Outline each blood parasite and name the species.
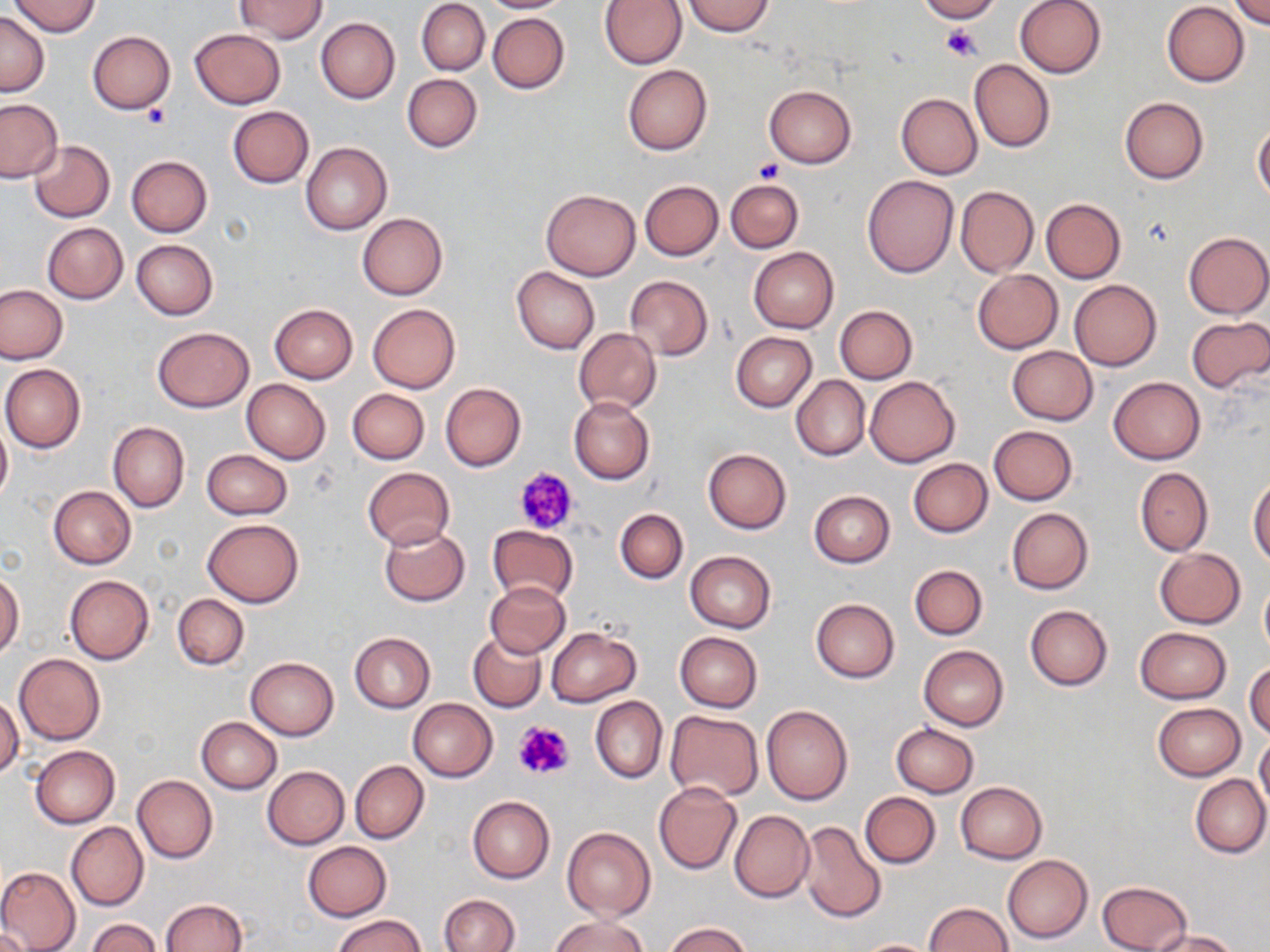

No blood parasites observed.

Approximate bounding boxes as named x1/y1/x2/y2 corners in pixels. Uninfected red blood cell locations: (x1=10, y1=0, x2=101, y2=36), (x1=233, y1=0, x2=328, y2=41), (x1=481, y1=0, x2=576, y2=12), (x1=917, y1=0, x2=1000, y2=23), (x1=1015, y1=0, x2=1107, y2=78), (x1=1232, y1=0, x2=1269, y2=28), (x1=417, y1=1, x2=489, y2=75), (x1=598, y1=1, x2=687, y2=68), (x1=683, y1=1, x2=775, y2=36), (x1=1162, y1=2, x2=1249, y2=86), (x1=0, y1=13, x2=49, y2=96), (x1=488, y1=13, x2=569, y2=93), (x1=315, y1=17, x2=400, y2=103), (x1=190, y1=27, x2=285, y2=109), (x1=87, y1=30, x2=175, y2=115), (x1=969, y1=59, x2=1054, y2=152), (x1=623, y1=65, x2=712, y2=154), (x1=402, y1=73, x2=481, y2=152), (x1=764, y1=85, x2=856, y2=167), (x1=896, y1=93, x2=982, y2=179), (x1=1118, y1=97, x2=1208, y2=184), (x1=0, y1=98, x2=63, y2=183), (x1=228, y1=107, x2=314, y2=188), (x1=1253, y1=123, x2=1270, y2=202), (x1=28, y1=140, x2=115, y2=222), (x1=301, y1=142, x2=392, y2=235), (x1=126, y1=155, x2=212, y2=236), (x1=863, y1=175, x2=959, y2=278), (x1=725, y1=179, x2=804, y2=253), (x1=640, y1=180, x2=723, y2=260), (x1=955, y1=185, x2=1037, y2=278), (x1=541, y1=188, x2=640, y2=280), (x1=1041, y1=198, x2=1125, y2=283), (x1=358, y1=212, x2=447, y2=300), (x1=41, y1=222, x2=128, y2=304), (x1=1183, y1=231, x2=1269, y2=319), (x1=131, y1=240, x2=218, y2=320), (x1=750, y1=247, x2=838, y2=333), (x1=511, y1=267, x2=600, y2=355), (x1=973, y1=269, x2=1063, y2=354), (x1=625, y1=276, x2=712, y2=360), (x1=1069, y1=279, x2=1162, y2=371), (x1=0, y1=284, x2=69, y2=364), (x1=368, y1=303, x2=461, y2=392), (x1=269, y1=304, x2=357, y2=384), (x1=835, y1=305, x2=917, y2=383), (x1=1186, y1=316, x2=1270, y2=393), (x1=152, y1=327, x2=253, y2=412), (x1=574, y1=328, x2=661, y2=413), (x1=731, y1=333, x2=816, y2=411), (x1=1007, y1=346, x2=1097, y2=426), (x1=1, y1=364, x2=85, y2=452), (x1=791, y1=375, x2=869, y2=461), (x1=865, y1=375, x2=960, y2=468), (x1=1109, y1=376, x2=1205, y2=464), (x1=242, y1=378, x2=331, y2=464), (x1=439, y1=382, x2=526, y2=472), (x1=347, y1=388, x2=429, y2=464), (x1=568, y1=397, x2=654, y2=484), (x1=0, y1=419, x2=11, y2=504), (x1=108, y1=422, x2=189, y2=512), (x1=988, y1=426, x2=1078, y2=505), (x1=703, y1=448, x2=791, y2=534), (x1=202, y1=449, x2=292, y2=519), (x1=908, y1=459, x2=992, y2=538), (x1=1134, y1=466, x2=1212, y2=556), (x1=362, y1=467, x2=455, y2=549), (x1=1249, y1=476, x2=1270, y2=567), (x1=49, y1=487, x2=136, y2=569), (x1=809, y1=491, x2=895, y2=567), (x1=614, y1=508, x2=688, y2=583), (x1=1007, y1=508, x2=1093, y2=594), (x1=202, y1=519, x2=303, y2=607), (x1=380, y1=522, x2=470, y2=606), (x1=488, y1=525, x2=578, y2=605), (x1=1154, y1=548, x2=1247, y2=628), (x1=686, y1=552, x2=775, y2=633), (x1=910, y1=565, x2=987, y2=640), (x1=0, y1=571, x2=24, y2=659), (x1=65, y1=575, x2=154, y2=664), (x1=1259, y1=577, x2=1270, y2=660), (x1=485, y1=581, x2=570, y2=658), (x1=172, y1=594, x2=248, y2=670), (x1=811, y1=598, x2=899, y2=683), (x1=1025, y1=604, x2=1112, y2=690), (x1=1135, y1=626, x2=1231, y2=703), (x1=547, y1=627, x2=641, y2=707), (x1=467, y1=631, x2=546, y2=712), (x1=674, y1=631, x2=762, y2=713), (x1=350, y1=632, x2=435, y2=711), (x1=919, y1=645, x2=1009, y2=730), (x1=14, y1=654, x2=105, y2=745), (x1=245, y1=657, x2=338, y2=741), (x1=1247, y1=661, x2=1270, y2=742), (x1=0, y1=696, x2=23, y2=779), (x1=591, y1=696, x2=667, y2=783), (x1=408, y1=698, x2=497, y2=781), (x1=1153, y1=702, x2=1246, y2=780), (x1=762, y1=706, x2=852, y2=805), (x1=664, y1=710, x2=765, y2=802), (x1=197, y1=717, x2=281, y2=793), (x1=892, y1=722, x2=978, y2=797), (x1=1254, y1=735, x2=1270, y2=813), (x1=31, y1=746, x2=119, y2=828), (x1=350, y1=760, x2=428, y2=843), (x1=263, y1=766, x2=349, y2=849), (x1=133, y1=775, x2=218, y2=863), (x1=1190, y1=775, x2=1269, y2=858), (x1=956, y1=782, x2=1046, y2=863), (x1=654, y1=783, x2=742, y2=873), (x1=860, y1=791, x2=940, y2=868), (x1=468, y1=795, x2=554, y2=882), (x1=728, y1=810, x2=814, y2=902), (x1=798, y1=820, x2=886, y2=924), (x1=66, y1=821, x2=147, y2=911), (x1=562, y1=827, x2=655, y2=922), (x1=302, y1=841, x2=391, y2=921), (x1=1004, y1=855, x2=1093, y2=943), (x1=0, y1=866, x2=80, y2=952), (x1=1098, y1=880, x2=1192, y2=952), (x1=440, y1=894, x2=519, y2=951), (x1=160, y1=899, x2=246, y2=952), (x1=923, y1=902, x2=1014, y2=952), (x1=332, y1=913, x2=426, y2=952), (x1=548, y1=914, x2=650, y2=952), (x1=89, y1=919, x2=161, y2=952), (x1=663, y1=922, x2=754, y2=952), (x1=0, y1=928, x2=32, y2=951), (x1=1150, y1=929, x2=1240, y2=952), (x1=853, y1=938, x2=940, y2=951). Platelet locations: (x1=942, y1=25, x2=982, y2=60), (x1=141, y1=102, x2=169, y2=127), (x1=754, y1=158, x2=783, y2=183), (x1=515, y1=466, x2=579, y2=535), (x1=513, y1=720, x2=575, y2=781). Slide-level diagnosis: no evidence of blood parasites. Image is 1270×952 pixels. Thin blood smear. Optical microscopy. 1000x magnification. May-Grünwald-Giemsa-stained preparation. One field of a larger specimen.